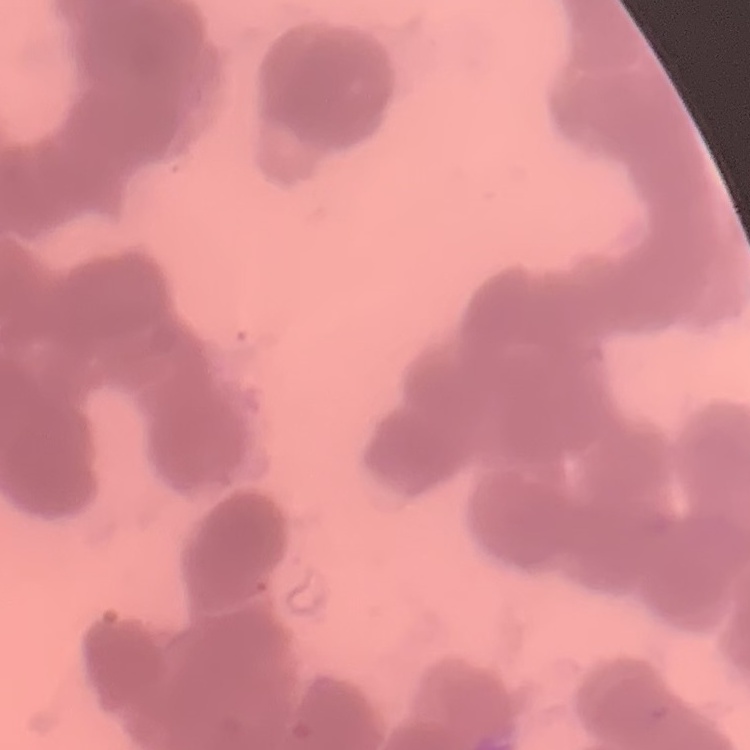 The red blood cells show rouleaux formation. Stained with either Field's or Giemsa. Square crop of a larger photomicrograph. Thin peripheral smear.